Classify this cell by malaria status.
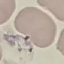

Uninfected.

{
  "capture": "smartphone through the microscope eyepiece",
  "image_type": "cell patch, automatically extracted from a larger field of view and resized to 64 × 64 pixels",
  "stain": "Giemsa",
  "preparation": "thin blood smear"
}